Identify the parasite.
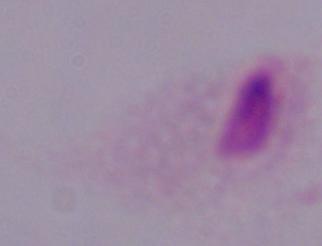
This is a trichomonad.

Summary:
  - Modality: photomicrograph
  - Magnification: 1000x